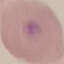
{
  "malaria_status": "uninfected",
  "image_type": "cell patch, automatically extracted from a larger field of view and resized to 64 × 64 pixels",
  "capture": "smartphone camera at the microscope eyepiece",
  "stain": "Giemsa",
  "preparation": "thin blood smear"
}